Report the malaria status of this cell.
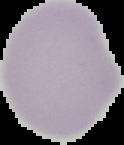

Uninfected.

Image is 124×145 pixels. Cell region segmented out of the field of view; the surrounding area is masked to black. From a thin blood film.